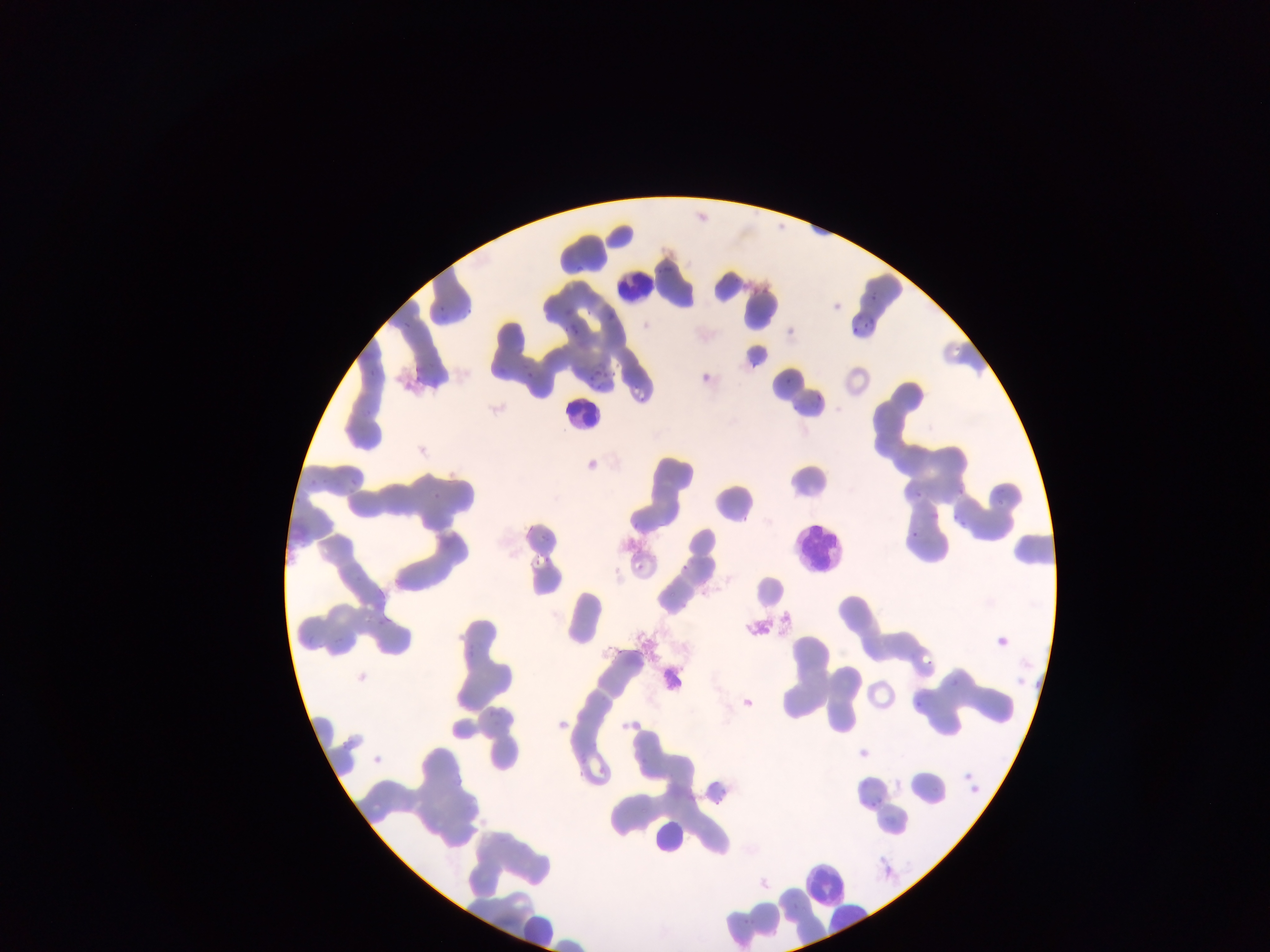
capture: mobile-phone photograph through a microscope
country: Ghana
image_size: 1270×952 pixels
field_of_view: single
plasmodium_parasite_locations: 'approximate bounding boxes as left top right bottom in pixels: 575 263 587 273; 861 289 878 304; 436 304 443 313; 463 306 474 315; 602 309 618 320; 851 312 861 320; 865 317 876 330; 403 318 415 329; 567 318 580 336; 847 326 856 335; 416 335 448 383; 366 356 382 377; 590 365 609 379; 521 366 536 381; 779 368 792 382; 812 390 823 407; 788 398 803 408; 348 402 373 426; 301 470 323 487; 349 472 360 491; 431 485 446 501; 911 485 920 499; 288 488 305 508; 953 488 964 497; 993 490 1008 504; 931 507 944 517; 950 509 967 529; 909 527 920 537; 533 544 552 570; 674 554 689 569; 630 559 639 570; 354 568 369 579; 992 639 1006 650; 923 656 934 673; 949 673 973 691; 487 696 509 724; 915 696 925 708; 329 722 354 752; 376 741 388 763; 964 767 974 780; 972 785 985 799; 715 786 732 808; 868 797 879 808; 790 896 801 913; 742 903 757 928'
preparation: thin blood smear
leukocyte_locations: 'approximate bounding boxes as left top right bottom in pixels: 607 260 655 308; 558 385 611 442; 790 519 838 570; 646 813 691 853; 799 847 842 903; 524 918 559 950'